Assess this cell for malaria.
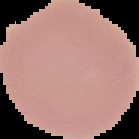

It is uninfected.

Summary:
  - Preparation: thin blood film
  - Image type: segmented cell region on a black background
  - Image size: 139×139 pixels